Classify this cell by malaria status.
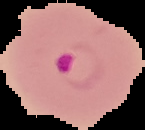
It is parasitized.

image size = 145×130 pixels
preparation = thin blood film
image type = segmented cell region with the area outside set to black